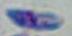

identification = Toxoplasma gondii
magnification = 1000x
modality = micrograph